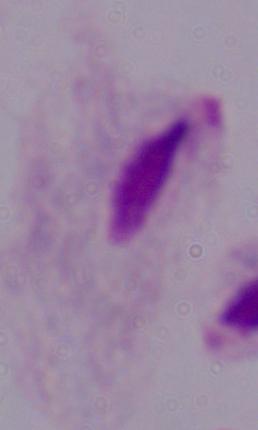
{
  "identification": "trichomonad",
  "magnification": "1000x",
  "modality": "micrograph"
}